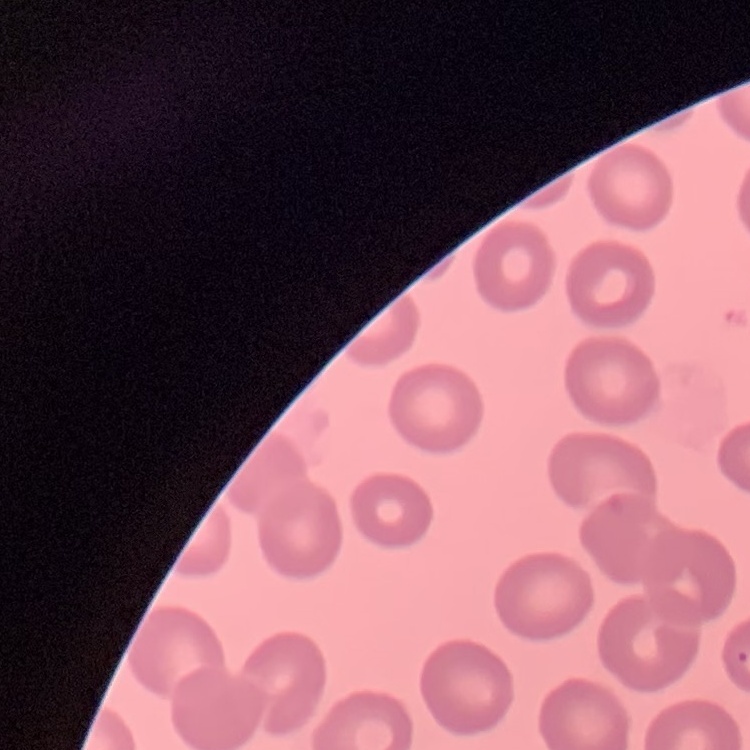
Summary:
  - Erythrocyte morphology: no rouleaux formation
  - Stain: Field's or Giemsa
  - Image type: square crop of a larger photomicrograph
  - Preparation: thin blood smear